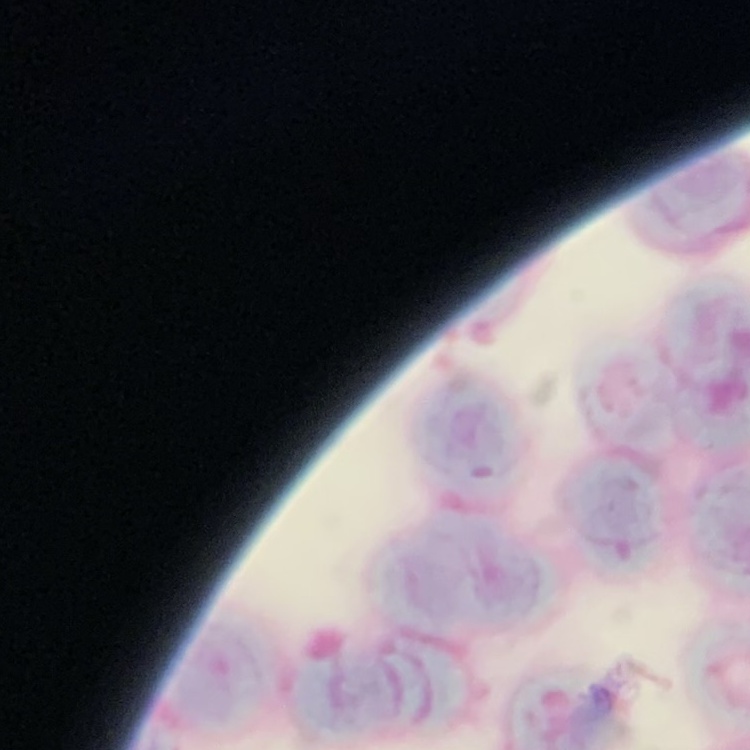

red blood cell morphology = rouleaux formation
stain = Field's or Giemsa
preparation = thin peripheral smear
image type = one tile cut from a larger photomicrograph